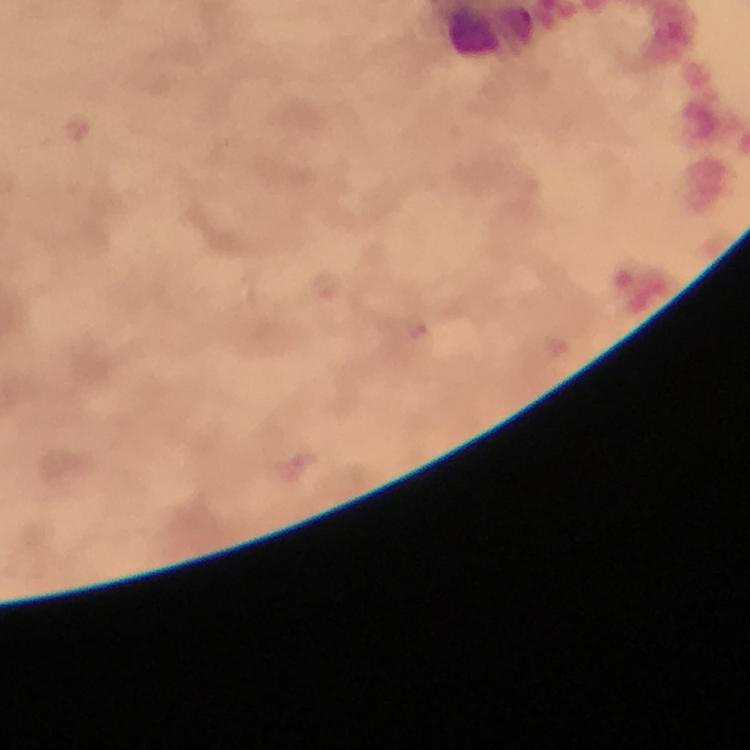 Approximate object centers, in pixels from the top-left corner. Plasmodium parasite locations: (x=326, y=288), (x=419, y=330). Immersion oil was used. Photographed through the microscope with a smartphone camera. Cropped region of a single field of view. 100x magnification. From a malaria diagnostic workup. Giemsa-stained preparation. Image is 750×750 pixels. Thick smear.